Locate and identify every blood parasite.
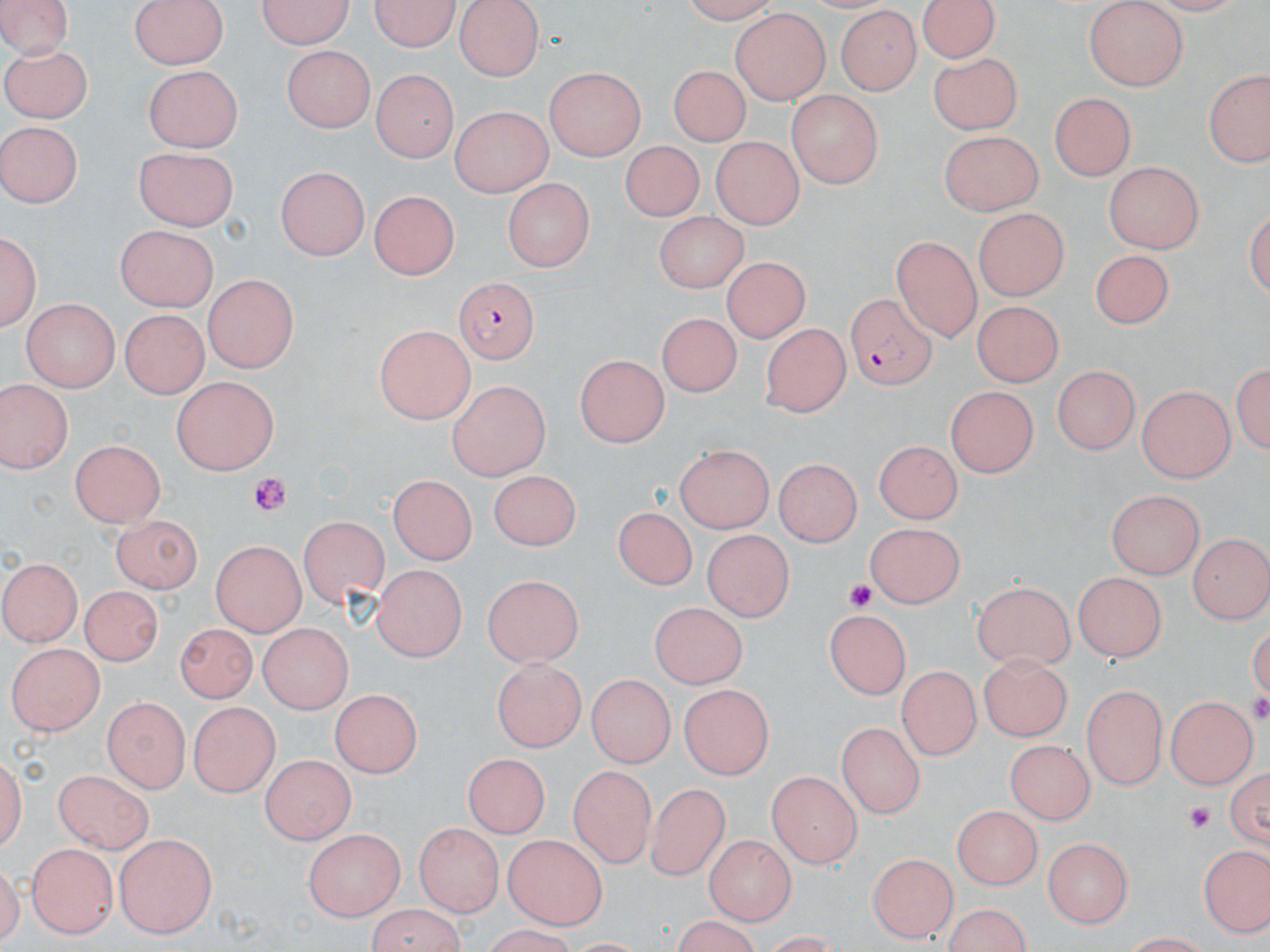

Approximate bounding boxes as (x1, y1, x2, y2) in pixels.
Plasmodium falciparum-infected red blood cells: (450, 277, 540, 364), (847, 292, 938, 391).
No Plasmodium ovale, Plasmodium malariae, Plasmodium vivax, Babesia divergens, or Trypanosoma brucei observed.

Summary:
  - Uninfected red blood cell locations: (0, 0, 76, 54), (129, 0, 229, 70), (254, 0, 357, 50), (372, 0, 458, 50), (454, 0, 546, 81), (671, 0, 780, 23), (915, 0, 1005, 64), (1085, 2, 1188, 91), (833, 7, 923, 96), (730, 10, 831, 104), (4, 38, 96, 120), (281, 46, 373, 133), (929, 56, 1021, 133), (141, 64, 245, 149), (668, 65, 749, 146), (542, 66, 646, 159), (1203, 66, 1270, 171), (369, 69, 458, 163), (788, 89, 881, 189), (1051, 92, 1132, 181), (449, 101, 552, 198), (2, 120, 83, 208), (939, 130, 1041, 219), (712, 134, 808, 227), (620, 139, 702, 224), (136, 145, 241, 229), (1103, 160, 1203, 254), (274, 167, 367, 261), (500, 179, 592, 270), (367, 188, 460, 279), (970, 205, 1068, 298), (653, 209, 750, 295), (1, 224, 41, 333), (116, 226, 219, 311), (890, 239, 979, 341), (1093, 246, 1175, 329), (724, 255, 806, 344), (204, 271, 298, 372), (969, 293, 1064, 380), (20, 298, 116, 392), (661, 309, 744, 394), (117, 314, 204, 397), (760, 323, 850, 418), (373, 325, 472, 423), (574, 356, 672, 447), (1232, 356, 1268, 458), (1051, 366, 1143, 455), (169, 376, 279, 477), (0, 377, 72, 475), (444, 381, 552, 477), (1136, 385, 1233, 483), (944, 386, 1036, 479), (870, 435, 961, 521), (70, 438, 167, 525), (675, 446, 774, 535), (775, 455, 864, 545), (488, 470, 581, 550), (391, 475, 474, 566), (1107, 491, 1202, 580), (617, 506, 694, 592), (108, 509, 201, 593), (297, 516, 388, 609), (866, 519, 969, 606), (700, 530, 790, 624), (1187, 533, 1268, 624), (208, 542, 306, 634), (1, 557, 83, 647), (371, 566, 464, 663), (1075, 573, 1164, 663), (481, 574, 586, 662), (971, 580, 1073, 672), (82, 584, 165, 664), (651, 601, 748, 697), (824, 610, 911, 700), (175, 622, 254, 705), (257, 624, 354, 711), (5, 638, 103, 734), (978, 649, 1071, 741), (492, 657, 585, 751), (898, 669, 976, 760), (584, 670, 674, 768), (1083, 683, 1167, 792), (679, 684, 778, 775), (328, 688, 420, 779), (103, 696, 190, 792), (1169, 696, 1255, 791), (186, 700, 279, 796), (835, 720, 924, 820), (1004, 739, 1095, 825), (460, 752, 554, 835), (259, 754, 355, 842), (1227, 758, 1269, 855), (567, 763, 654, 864), (766, 768, 861, 865), (50, 770, 155, 851), (642, 783, 731, 880), (954, 805, 1045, 887), (415, 823, 502, 917), (298, 827, 408, 919), (112, 833, 216, 938), (503, 833, 609, 930), (703, 834, 795, 924), (1043, 835, 1132, 931), (1201, 841, 1270, 930), (26, 843, 117, 938), (863, 849, 953, 939), (362, 907, 470, 952)
  - Platelet locations: (245, 472, 296, 516), (843, 577, 878, 612), (1249, 692, 1270, 723), (1183, 798, 1221, 832)
  - Slide-level diagnosis: Plasmodium falciparum
  - Magnification: 1000x
  - Image size: 1270×952 pixels
  - Preparation: thin blood smear
  - Field of view: one of a larger specimen
  - Stain: May-Grünwald-Giemsa
  - Modality: light microscopy